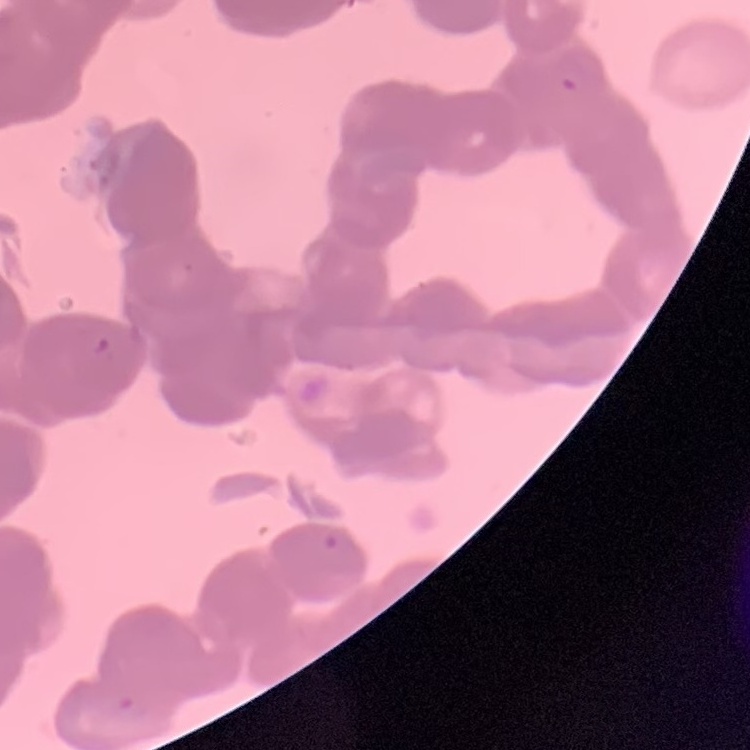

Summary:
  - Erythrocyte morphology: rouleaux formation
  - Image type: one tile cut from a larger photomicrograph
  - Preparation: thin peripheral smear
  - Stain: Field's or Giemsa